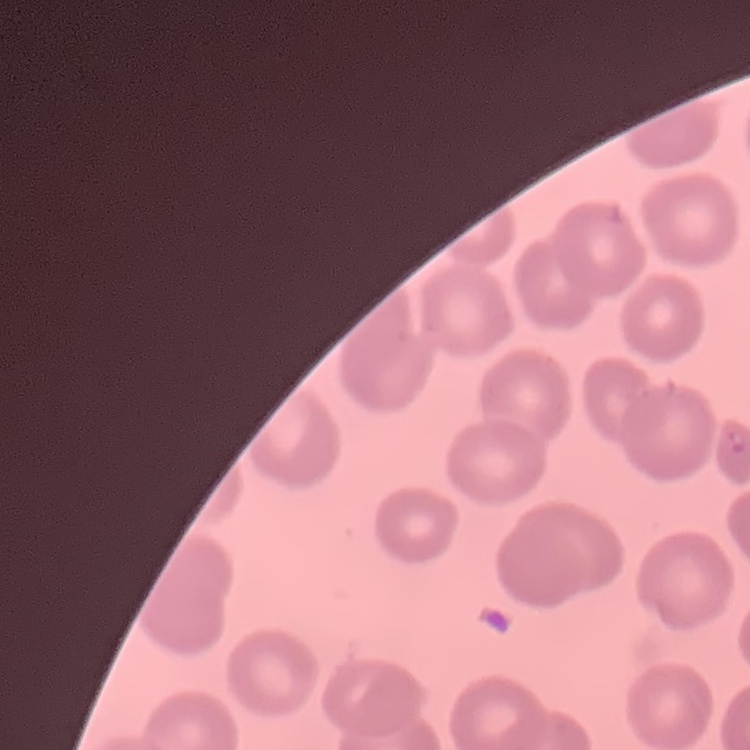
Summary:
  - Erythrocyte morphology: no rouleaux formation
  - Stain: Field's or Giemsa
  - Image type: square crop of a larger photomicrograph
  - Preparation: thin blood smear